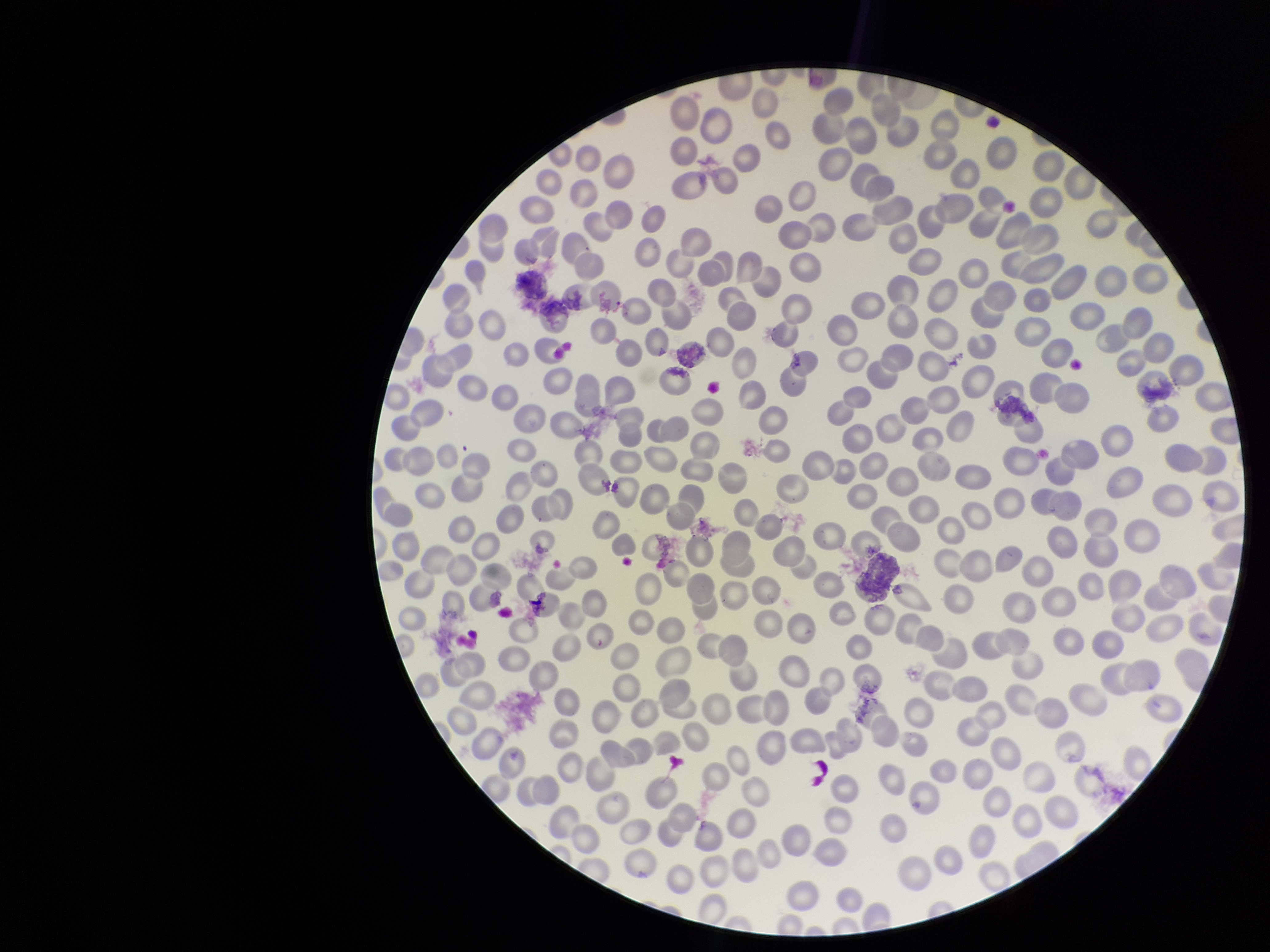 Patient malaria status: negative. Single field of view. Preparation: thin smear. Parasitized red blood cell count: 0. Stained with Giemsa. Red blood cell count: 298. Smartphone photograph taken through the eyepiece of a microscope. Parasitized red blood cells: none detected. Image is 1270×952 pixels.